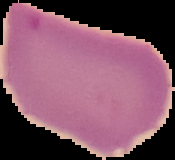 Image is 175×160 pixels. Result: no malaria parasites detected. The area outside the segmented cell region is set to black. From a thin blood smear.